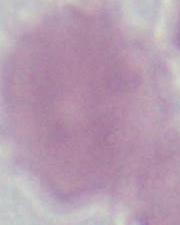
1000x magnification. Micrograph. A red blood cell is seen.